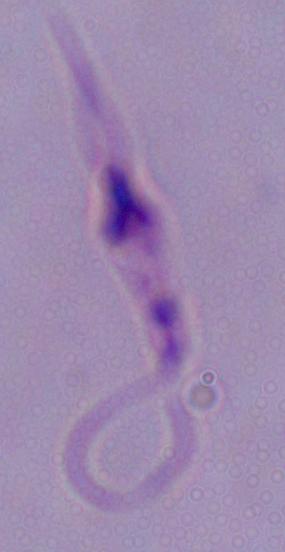

1000x magnification. Photomicrograph. A Leishmania parasite is seen.